Identify the blood parasite species.
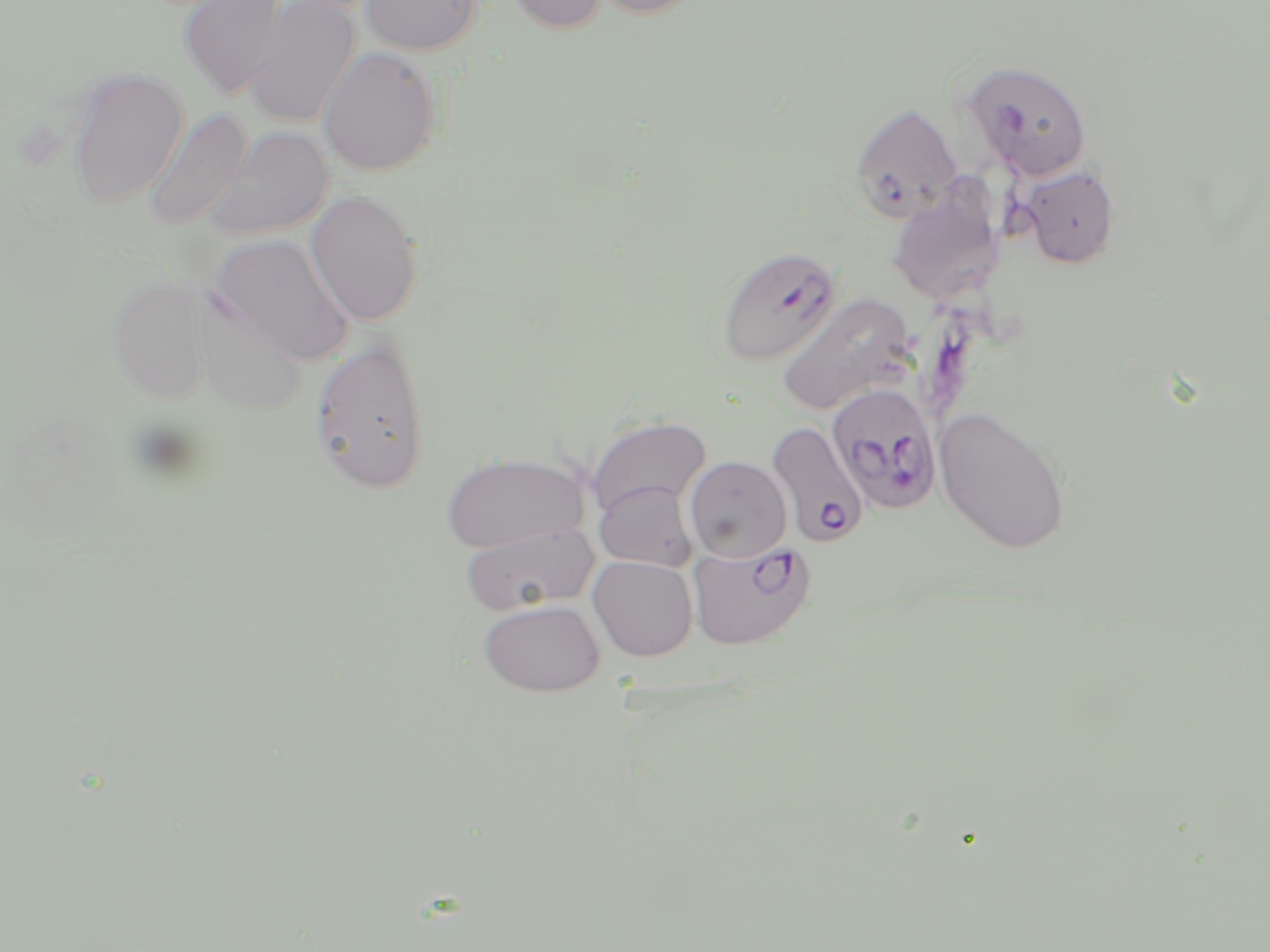

Plasmodium falciparum.

Summary:
  - Coordinate format: approximate bounding boxes as (x1, y1, x2, y2) in pixels
  - Plasmodium falciparum-infected red blood cell locations: (963, 59, 1092, 181), (849, 102, 964, 223), (716, 246, 841, 366), (826, 383, 943, 516), (766, 422, 868, 548), (687, 539, 816, 649)
  - Uninfected red blood cell locations: (178, 0, 287, 98), (244, 0, 360, 128), (361, 0, 483, 55), (506, 0, 608, 34), (590, 0, 702, 19), (318, 46, 442, 175), (66, 66, 189, 208), (144, 108, 251, 231), (205, 126, 334, 240), (1018, 164, 1121, 269), (887, 184, 1004, 306), (304, 189, 424, 327), (211, 233, 356, 365), (108, 274, 211, 405), (190, 291, 309, 417), (776, 292, 915, 416), (308, 335, 431, 495), (934, 404, 1071, 554), (585, 415, 711, 516), (441, 451, 589, 552), (684, 456, 792, 562), (594, 481, 698, 572), (458, 524, 600, 615), (588, 555, 698, 661), (478, 599, 605, 696)
  - Stain: May-Grünwald-Giemsa
  - Field of view: single
  - Image size: 1270×952 pixels
  - Magnification: 1000x
  - Modality: optical microscopy
  - Preparation: thin blood film